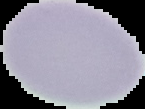
Summary:
  - Preparation: thin blood film
  - Image size: 145×109 pixels
  - Malaria status: uninfected
  - Image type: segmented cell region on a black background